Describe the morphology of the red blood cells.
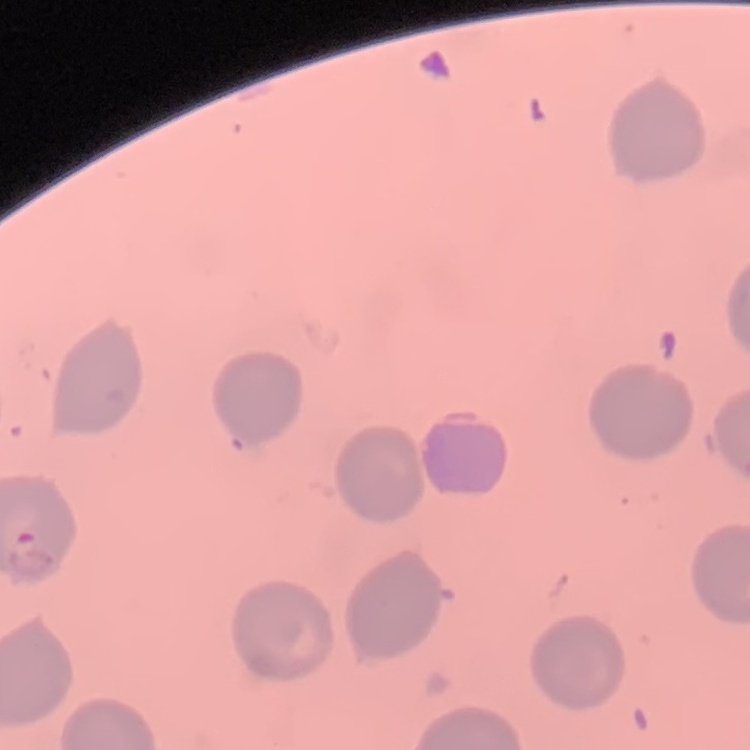
No rouleaux formation.

One tile cut from a larger photomicrograph. Thin blood film. Stained with either Field's or Giemsa.